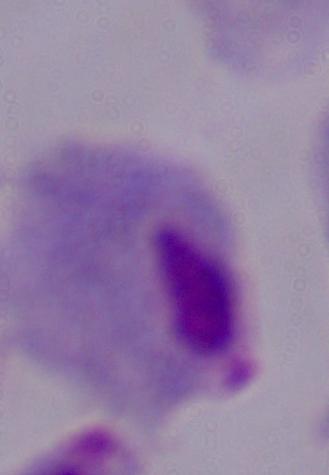 Photomicrograph. 1000x magnification. A trichomonad is shown.